Describe the morphology of the red blood cells.
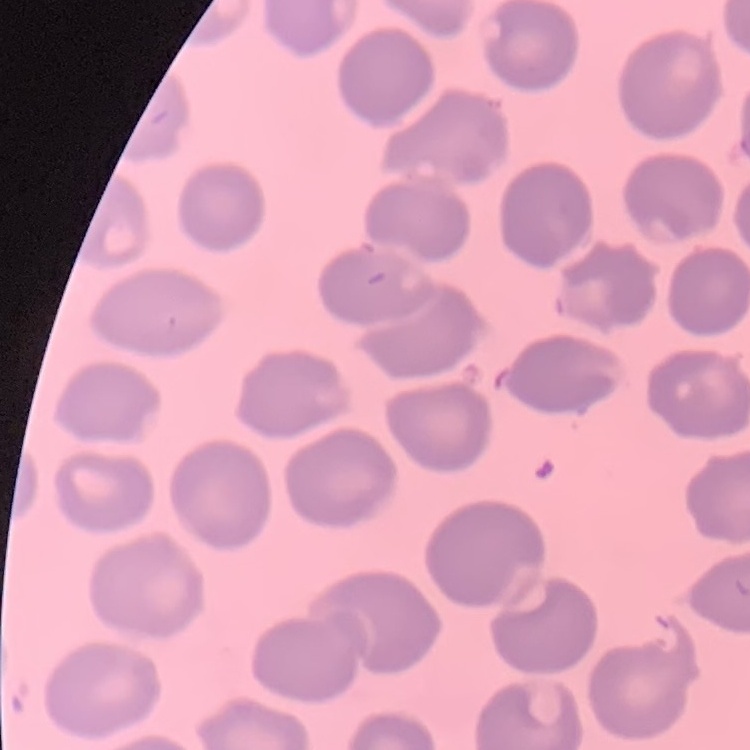

No rouleaux formation.

Summary:
  - Stain: Field's or Giemsa
  - Image type: one tile cut from a larger photomicrograph
  - Preparation: thin blood smear